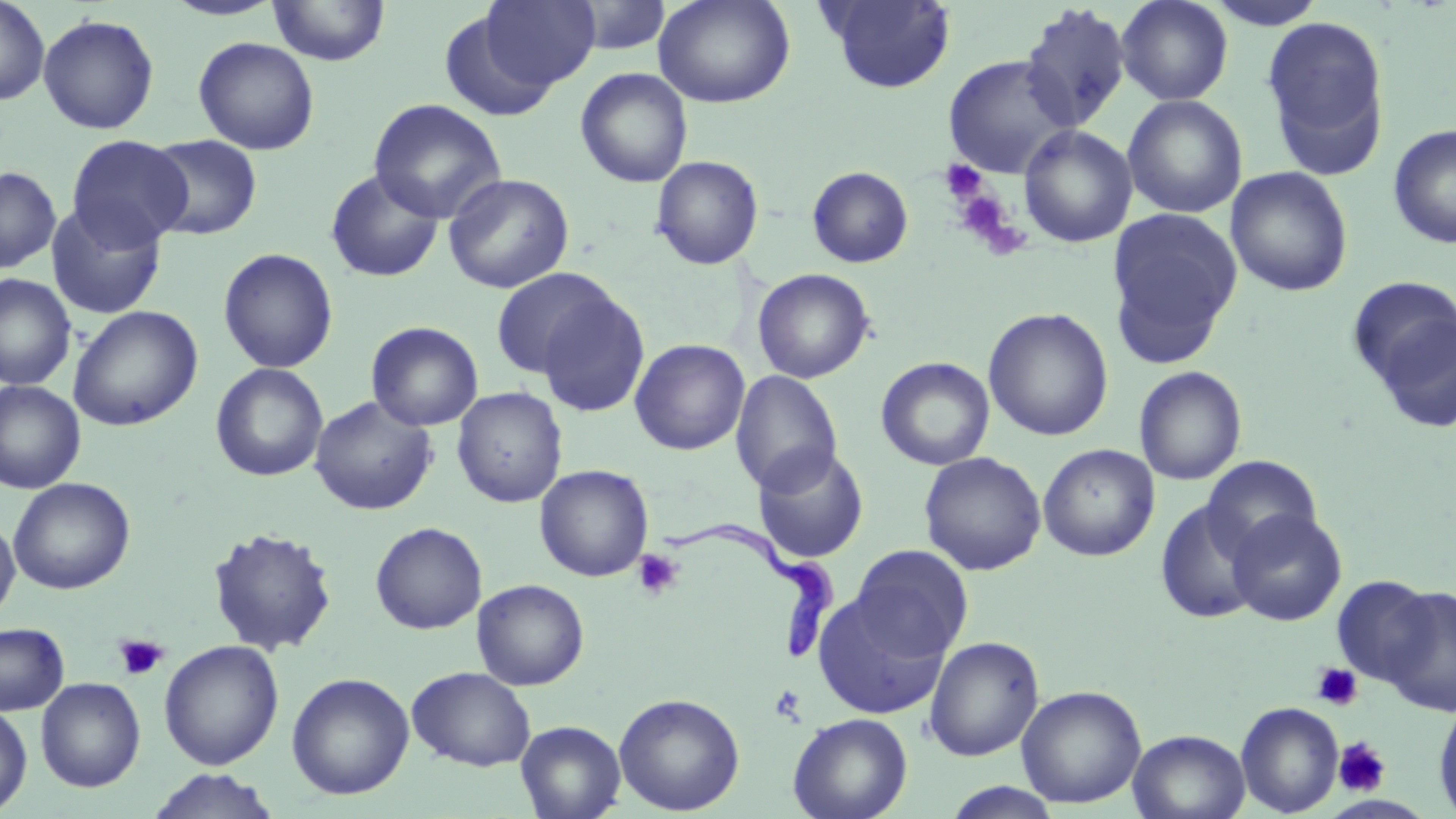
Summary:
  - Coordinate format: approximate bounding boxes as (x1, y1, x2, y2) in pixels
  - Trypanosoma brucei locations: (662, 525, 835, 666)
  - Uninfected red blood cell locations: (0, 0, 50, 107), (160, 0, 288, 22), (268, 0, 390, 66), (479, 0, 600, 90), (566, 0, 671, 55), (652, 0, 795, 108), (820, 0, 957, 93), (1116, 0, 1234, 105), (1204, 0, 1329, 30), (1019, 3, 1132, 133), (438, 8, 560, 121), (37, 14, 159, 135), (1261, 14, 1391, 177), (193, 36, 319, 155), (943, 54, 1076, 179), (575, 67, 693, 188), (1122, 95, 1247, 218), (368, 98, 507, 224), (1387, 124, 1456, 249), (1018, 125, 1138, 248), (145, 134, 262, 240), (66, 135, 192, 250), (650, 155, 764, 270), (807, 165, 913, 268), (0, 166, 61, 273), (1226, 166, 1353, 297), (324, 168, 445, 282), (443, 173, 574, 293), (45, 203, 166, 319), (1107, 208, 1242, 365), (218, 248, 339, 373), (490, 267, 620, 381), (752, 268, 875, 383), (0, 274, 76, 391), (1345, 276, 1456, 394), (532, 288, 651, 419), (68, 305, 203, 431), (983, 308, 1113, 441), (366, 321, 484, 432), (629, 338, 750, 455), (876, 357, 995, 471), (210, 363, 328, 481), (1134, 366, 1247, 486), (730, 371, 843, 495), (0, 380, 86, 494), (451, 386, 568, 507), (309, 395, 438, 515), (1038, 444, 1159, 561), (752, 445, 870, 563), (919, 451, 1047, 576), (1202, 454, 1322, 559), (534, 464, 654, 582), (9, 477, 136, 594), (1154, 500, 1265, 624), (1227, 509, 1346, 626), (0, 514, 20, 621), (370, 522, 487, 634), (207, 526, 339, 655), (850, 545, 973, 660), (1332, 576, 1438, 687), (471, 579, 590, 690), (1379, 585, 1456, 717), (813, 592, 951, 720), (0, 622, 69, 715), (924, 635, 1044, 761), (158, 640, 284, 770), (406, 666, 536, 771), (286, 672, 414, 800), (36, 677, 146, 792), (1016, 685, 1146, 808), (613, 692, 745, 815), (1433, 697, 1456, 819), (1236, 701, 1343, 816), (0, 703, 32, 815), (788, 712, 913, 819), (516, 720, 626, 819), (1128, 729, 1250, 819), (145, 769, 282, 819), (942, 782, 1063, 819)
  - Platelet locations: (940, 159, 987, 202), (950, 186, 1021, 252), (632, 549, 684, 599), (115, 633, 168, 682), (1311, 662, 1362, 712), (770, 684, 806, 724), (1333, 737, 1391, 796)
  - Slide-level diagnosis: Trypanosoma brucei
  - Field of view: single
  - Modality: light microscopy
  - Preparation: thin blood film
  - Stain: May-Grünwald-Giemsa
  - Magnification: 1000x
  - Image size: 1456×819 pixels